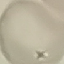

Result: negative for malaria parasites. Acquired by smartphone through the microscope eyepiece. Giemsa-stained preparation. Thin smear of blood. Cell patch, automatically extracted from a larger field of view and resized to 64 × 64 pixels.